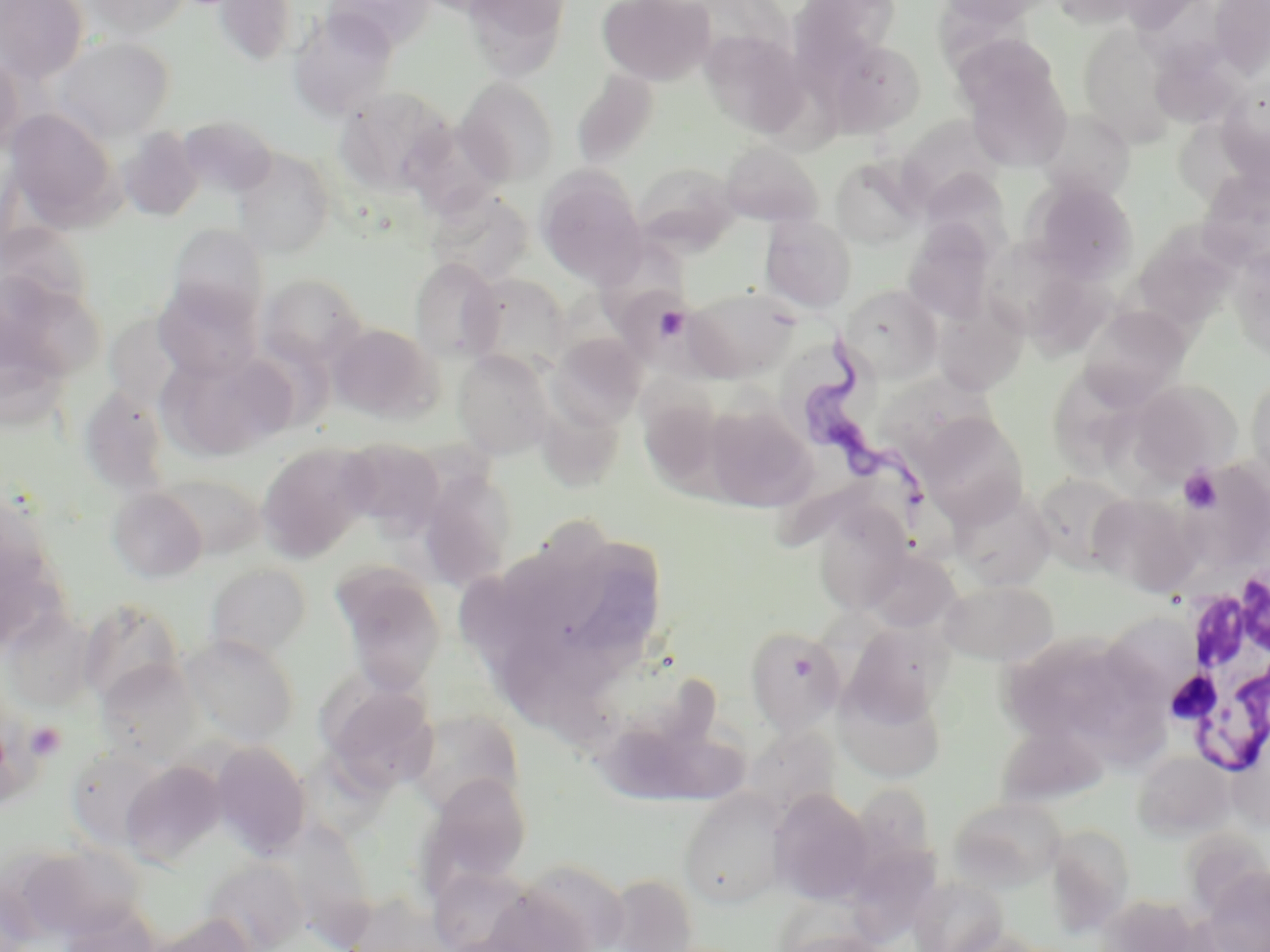

{
  "trypanosoma_brucei_locations": "approximate bounding boxes as named x1/y1/x2/y2 corners in pixels: (x1=802, y1=330, x2=935, y2=519)",
  "slide_level_diagnosis": "Trypanosoma brucei",
  "magnification": "1000x",
  "image_size": "1270×952 pixels",
  "modality": "optical microscopy",
  "stain": "May-Grünwald-Giemsa",
  "preparation": "thin blood smear",
  "field_of_view": "one of a larger specimen",
  "platelet_locations": "approximate bounding boxes as named x1/y1/x2/y2 corners in pixels: (x1=1179, y1=467, x2=1222, y2=513), (x1=25, y1=722, x2=66, y2=761)",
  "white_blood_cell_locations": "approximate bounding boxes as named x1/y1/x2/y2 corners in pixels: (x1=1162, y1=568, x2=1270, y2=779)",
  "uninfected_red_blood_cell_locations": "approximate bounding boxes as named x1/y1/x2/y2 corners in pixels: (x1=0, y1=0, x2=88, y2=84), (x1=81, y1=0, x2=192, y2=40), (x1=212, y1=0, x2=300, y2=67), (x1=322, y1=0, x2=435, y2=53), (x1=462, y1=0, x2=572, y2=81), (x1=597, y1=0, x2=716, y2=86), (x1=788, y1=0, x2=904, y2=74), (x1=939, y1=0, x2=1054, y2=26), (x1=1051, y1=0, x2=1150, y2=28), (x1=1209, y1=1, x2=1270, y2=77), (x1=288, y1=9, x2=398, y2=122), (x1=1077, y1=24, x2=1177, y2=144), (x1=699, y1=29, x2=810, y2=140), (x1=955, y1=34, x2=1062, y2=125), (x1=51, y1=36, x2=175, y2=142), (x1=825, y1=39, x2=926, y2=137), (x1=0, y1=48, x2=25, y2=155), (x1=964, y1=63, x2=1072, y2=171), (x1=572, y1=69, x2=660, y2=170), (x1=455, y1=77, x2=560, y2=188), (x1=1217, y1=82, x2=1270, y2=179), (x1=334, y1=86, x2=455, y2=196), (x1=4, y1=108, x2=120, y2=229), (x1=1036, y1=108, x2=1135, y2=201), (x1=898, y1=115, x2=1003, y2=206), (x1=118, y1=127, x2=204, y2=223), (x1=719, y1=142, x2=825, y2=229), (x1=232, y1=149, x2=335, y2=258), (x1=830, y1=156, x2=927, y2=250), (x1=632, y1=162, x2=740, y2=252), (x1=1199, y1=165, x2=1270, y2=270), (x1=535, y1=167, x2=648, y2=288), (x1=920, y1=169, x2=1013, y2=256), (x1=1028, y1=179, x2=1139, y2=282), (x1=424, y1=189, x2=535, y2=287), (x1=760, y1=215, x2=857, y2=313), (x1=903, y1=220, x2=997, y2=324), (x1=0, y1=221, x2=93, y2=318), (x1=167, y1=223, x2=269, y2=325), (x1=1140, y1=229, x2=1240, y2=335), (x1=595, y1=233, x2=690, y2=339), (x1=1228, y1=246, x2=1270, y2=361), (x1=999, y1=255, x2=1120, y2=365), (x1=409, y1=258, x2=503, y2=362), (x1=257, y1=272, x2=367, y2=369), (x1=0, y1=273, x2=103, y2=397), (x1=463, y1=273, x2=571, y2=376), (x1=153, y1=280, x2=263, y2=382), (x1=841, y1=285, x2=942, y2=382), (x1=684, y1=286, x2=798, y2=381), (x1=933, y1=304, x2=1029, y2=397), (x1=1078, y1=304, x2=1191, y2=410), (x1=103, y1=306, x2=217, y2=421), (x1=327, y1=322, x2=441, y2=422), (x1=547, y1=332, x2=647, y2=430), (x1=154, y1=348, x2=296, y2=462), (x1=452, y1=349, x2=555, y2=459), (x1=643, y1=362, x2=723, y2=476), (x1=1054, y1=365, x2=1143, y2=473), (x1=1245, y1=373, x2=1270, y2=490), (x1=1126, y1=379, x2=1239, y2=481), (x1=82, y1=387, x2=169, y2=485), (x1=533, y1=391, x2=626, y2=491), (x1=702, y1=402, x2=817, y2=511), (x1=917, y1=413, x2=1030, y2=525), (x1=340, y1=439, x2=445, y2=536), (x1=255, y1=442, x2=376, y2=563), (x1=1191, y1=459, x2=1270, y2=573), (x1=418, y1=470, x2=518, y2=589), (x1=1032, y1=472, x2=1135, y2=570), (x1=107, y1=486, x2=209, y2=583), (x1=950, y1=486, x2=1057, y2=591), (x1=1089, y1=493, x2=1198, y2=596), (x1=813, y1=505, x2=913, y2=614), (x1=863, y1=550, x2=959, y2=632), (x1=205, y1=563, x2=312, y2=662), (x1=331, y1=564, x2=447, y2=695), (x1=940, y1=580, x2=1058, y2=666), (x1=79, y1=599, x2=184, y2=708), (x1=2, y1=608, x2=97, y2=711), (x1=745, y1=626, x2=846, y2=734), (x1=1000, y1=631, x2=1168, y2=763), (x1=181, y1=634, x2=300, y2=746), (x1=96, y1=660, x2=203, y2=766), (x1=835, y1=674, x2=948, y2=783), (x1=321, y1=679, x2=438, y2=794), (x1=404, y1=708, x2=524, y2=815), (x1=991, y1=725, x2=1120, y2=809), (x1=210, y1=741, x2=311, y2=858), (x1=1133, y1=751, x2=1234, y2=841), (x1=120, y1=759, x2=227, y2=868), (x1=420, y1=772, x2=533, y2=891), (x1=858, y1=782, x2=936, y2=888), (x1=678, y1=788, x2=790, y2=910), (x1=768, y1=789, x2=874, y2=904), (x1=948, y1=796, x2=1067, y2=892), (x1=286, y1=823, x2=375, y2=950), (x1=1046, y1=823, x2=1135, y2=934), (x1=24, y1=843, x2=151, y2=938), (x1=850, y1=849, x2=947, y2=946), (x1=498, y1=857, x2=633, y2=952), (x1=202, y1=858, x2=307, y2=952), (x1=1204, y1=866, x2=1270, y2=952), (x1=601, y1=872, x2=699, y2=952), (x1=0, y1=882, x2=37, y2=952), (x1=149, y1=913, x2=257, y2=952)"
}